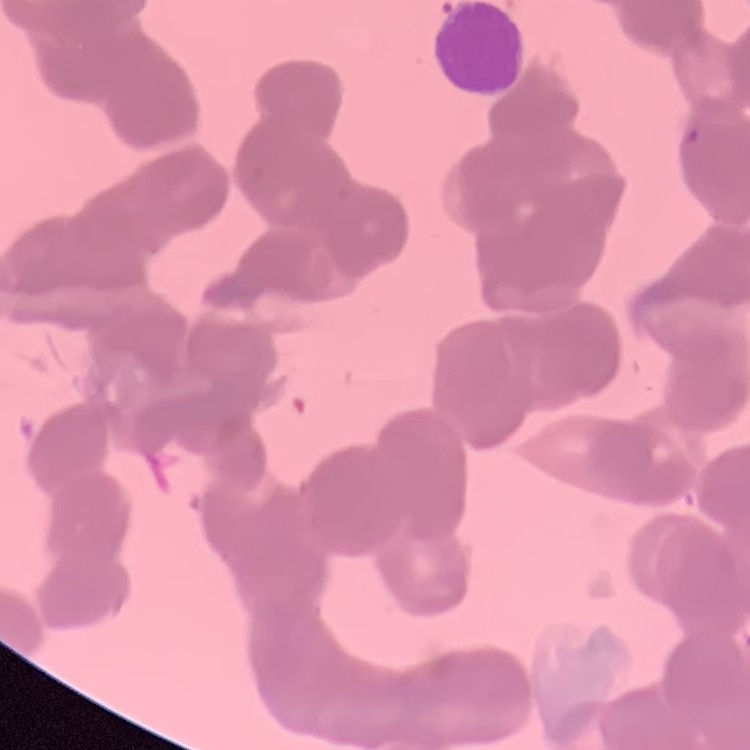

red blood cell morphology = rouleaux formation
preparation = thin blood smear
image type = one tile cut from a larger photomicrograph
stain = Field's or Giemsa